State the blood parasite species.
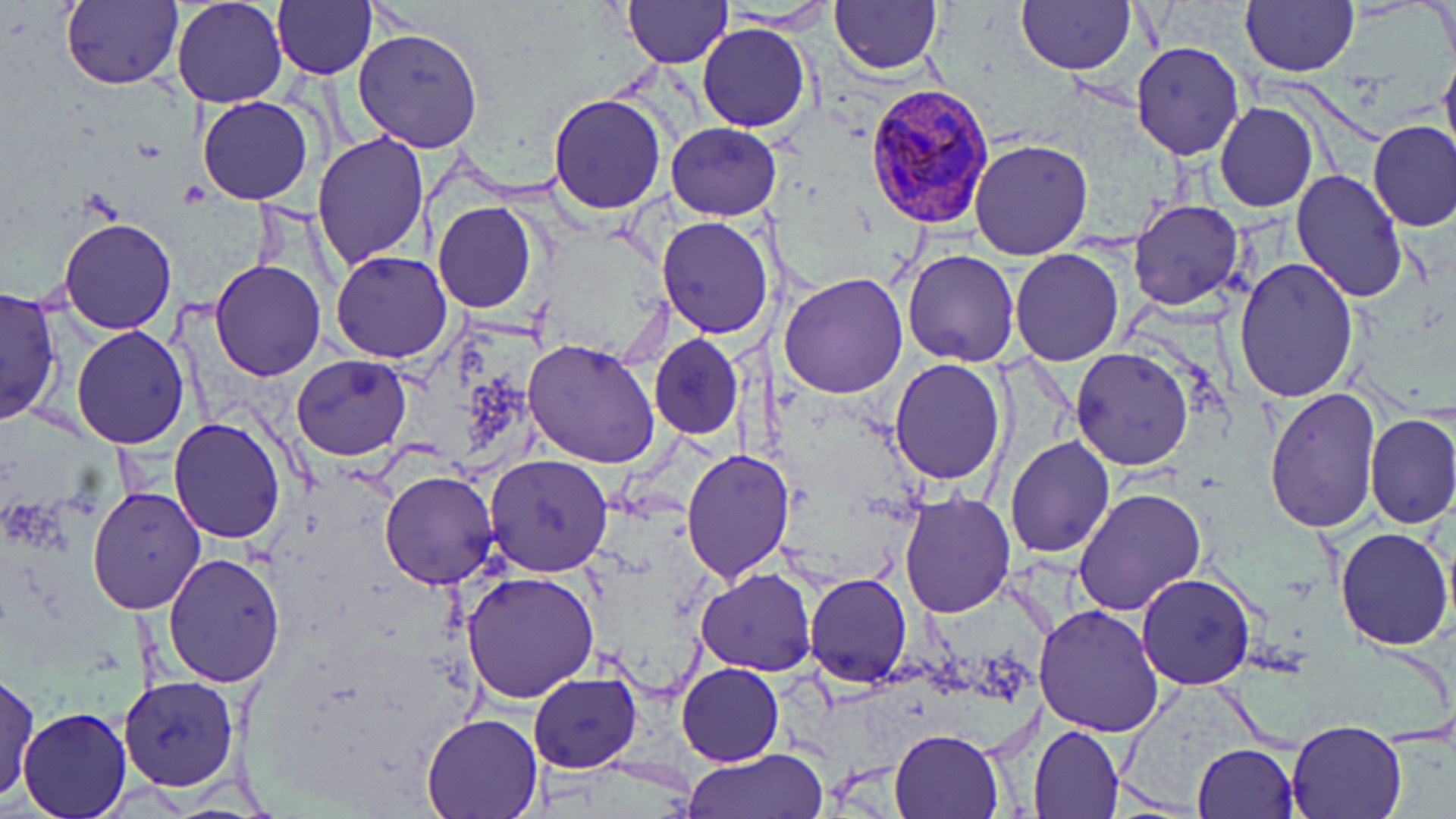
Plasmodium vivax.

Approximate bounding boxes as named x1/y1/x2/y2 corners in pixels. Uninfected red blood cell locations: (x1=61, y1=0, x2=182, y2=90), (x1=171, y1=0, x2=287, y2=108), (x1=272, y1=0, x2=375, y2=80), (x1=624, y1=0, x2=729, y2=67), (x1=828, y1=0, x2=943, y2=75), (x1=1240, y1=0, x2=1360, y2=77), (x1=1429, y1=0, x2=1454, y2=67), (x1=1016, y1=1, x2=1136, y2=73), (x1=184, y1=2, x2=297, y2=206), (x1=716, y1=5, x2=838, y2=35), (x1=695, y1=23, x2=810, y2=132), (x1=353, y1=26, x2=484, y2=152), (x1=1130, y1=41, x2=1244, y2=161), (x1=1439, y1=45, x2=1456, y2=168), (x1=548, y1=94, x2=667, y2=214), (x1=196, y1=96, x2=313, y2=205), (x1=1215, y1=101, x2=1318, y2=214), (x1=665, y1=121, x2=783, y2=220), (x1=1367, y1=122, x2=1456, y2=232), (x1=312, y1=132, x2=429, y2=269), (x1=968, y1=138, x2=1093, y2=260), (x1=1291, y1=166, x2=1410, y2=302), (x1=1129, y1=199, x2=1245, y2=312), (x1=432, y1=202, x2=537, y2=312), (x1=57, y1=216, x2=177, y2=335), (x1=655, y1=216, x2=775, y2=338), (x1=1008, y1=248, x2=1125, y2=367), (x1=901, y1=249, x2=1019, y2=366), (x1=330, y1=250, x2=454, y2=364), (x1=1234, y1=256, x2=1360, y2=403), (x1=209, y1=260, x2=327, y2=380), (x1=779, y1=272, x2=909, y2=399), (x1=0, y1=285, x2=61, y2=428), (x1=71, y1=325, x2=192, y2=448), (x1=649, y1=332, x2=743, y2=439), (x1=522, y1=338, x2=661, y2=467), (x1=1071, y1=346, x2=1194, y2=470), (x1=290, y1=354, x2=410, y2=459), (x1=890, y1=357, x2=1006, y2=486), (x1=1264, y1=387, x2=1380, y2=532), (x1=1364, y1=411, x2=1456, y2=529), (x1=169, y1=417, x2=286, y2=542), (x1=1005, y1=434, x2=1114, y2=556), (x1=680, y1=446, x2=794, y2=583), (x1=483, y1=453, x2=614, y2=576), (x1=379, y1=470, x2=500, y2=589), (x1=87, y1=483, x2=206, y2=614), (x1=1074, y1=485, x2=1206, y2=617), (x1=899, y1=490, x2=1015, y2=618), (x1=1332, y1=525, x2=1454, y2=649), (x1=163, y1=552, x2=286, y2=687), (x1=463, y1=569, x2=599, y2=704), (x1=696, y1=569, x2=817, y2=675), (x1=805, y1=574, x2=911, y2=687), (x1=1136, y1=574, x2=1255, y2=690), (x1=1033, y1=604, x2=1167, y2=738), (x1=677, y1=662, x2=784, y2=766), (x1=1, y1=669, x2=38, y2=804), (x1=527, y1=672, x2=641, y2=772), (x1=117, y1=676, x2=237, y2=791), (x1=18, y1=708, x2=132, y2=818), (x1=423, y1=712, x2=543, y2=817), (x1=1285, y1=720, x2=1407, y2=818), (x1=1029, y1=724, x2=1124, y2=817), (x1=888, y1=729, x2=1005, y2=817), (x1=1192, y1=743, x2=1300, y2=819), (x1=685, y1=748, x2=828, y2=819). Plasmodium vivax-infected red blood cell locations: (x1=866, y1=87, x2=994, y2=230). May-Grünwald-Giemsa-stained preparation. Image is 1456×819 pixels. 1000x magnification. Thin blood smear. One field of a larger specimen. Light microscopy.